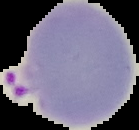

Summary:
  - Preparation: thin blood smear
  - Image size: 139×130 pixels
  - Image type: segmented cell region with the area outside set to black
  - Malaria status: parasitized